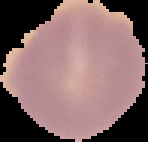
Summary:
  - Malaria status: uninfected
  - Image type: segmented cell region with the area outside set to black
  - Image size: 148×142 pixels
  - Preparation: thin blood film